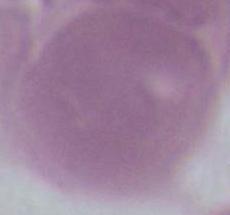

Summary:
  - Modality: micrograph
  - Magnification: 1000x
  - Identification: erythrocyte